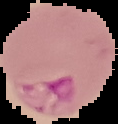
image_size: 118×124 pixels
preparation: thin blood smear
image_type: segmented cell region on a black background
malaria_status: parasitized